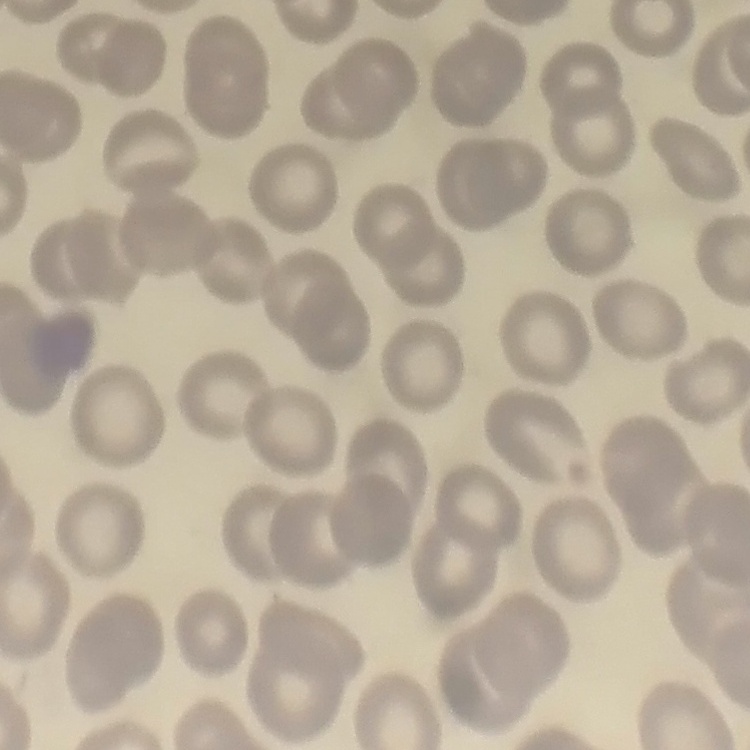
erythrocyte morphology = no rouleaux formation
stain = Field's or Giemsa
preparation = thin blood smear
image type = square crop of a larger photomicrograph